Outline each P. falciparum parasite and classify it by life-cycle stage.
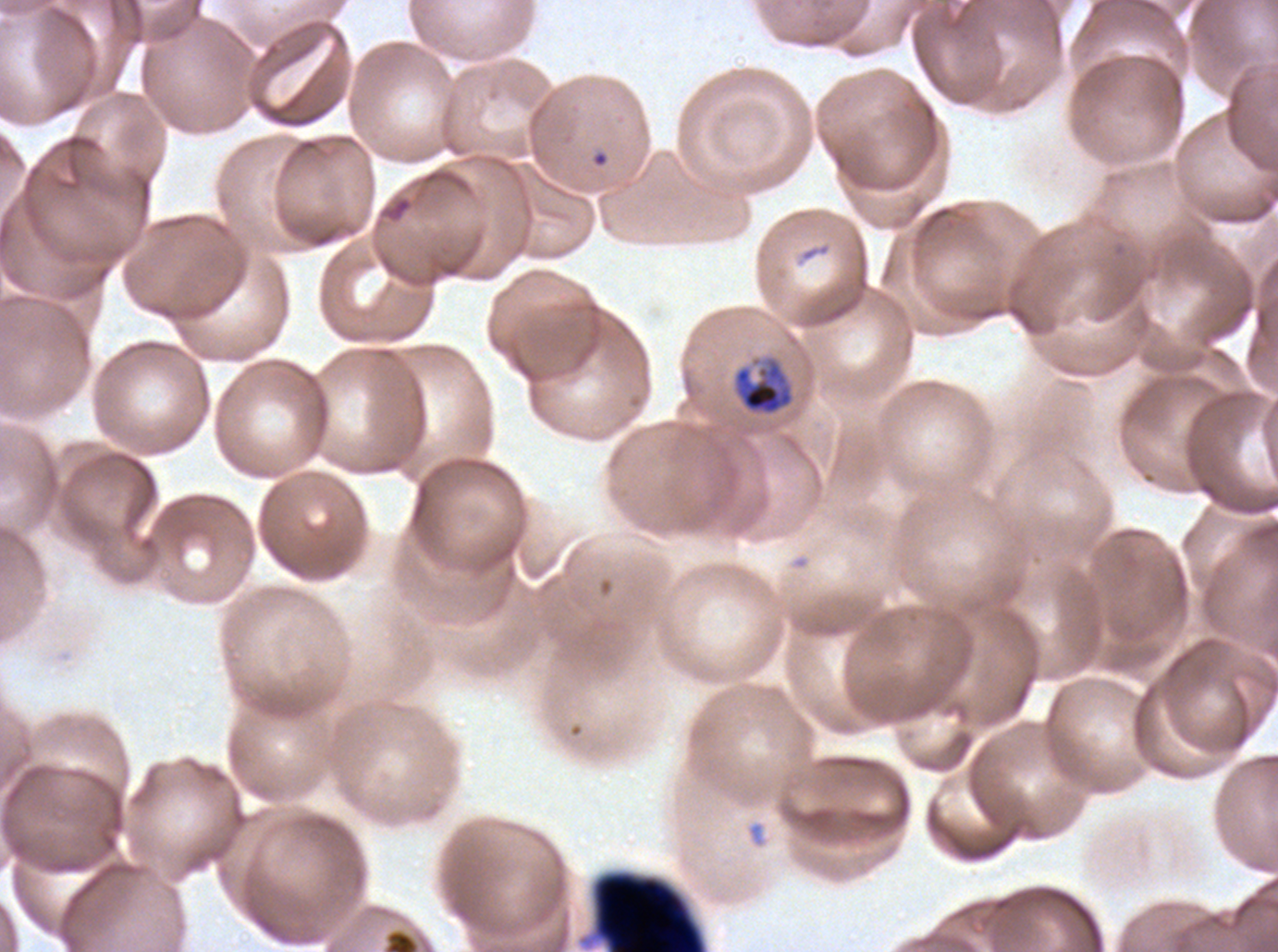

Approximate bounding boxes as [x1, y1, x2, y2] in pixels.
Mid trophozoites: [731, 354, 795, 417].
No rings, late-ring/early-trophozoite forms, late trophozoites, early schizonts, late schizonts, segmenters, or gametocytes observed.

debris locations = [584, 869, 708, 951]
field of view = one sub-image of a larger composite
specimen = P. falciparum cultured ex vivo for 24 to 48 hours, from a patient in The Gambia
preparation = thin blood smear
image size = 1278×952 pixels
stain = Giemsa